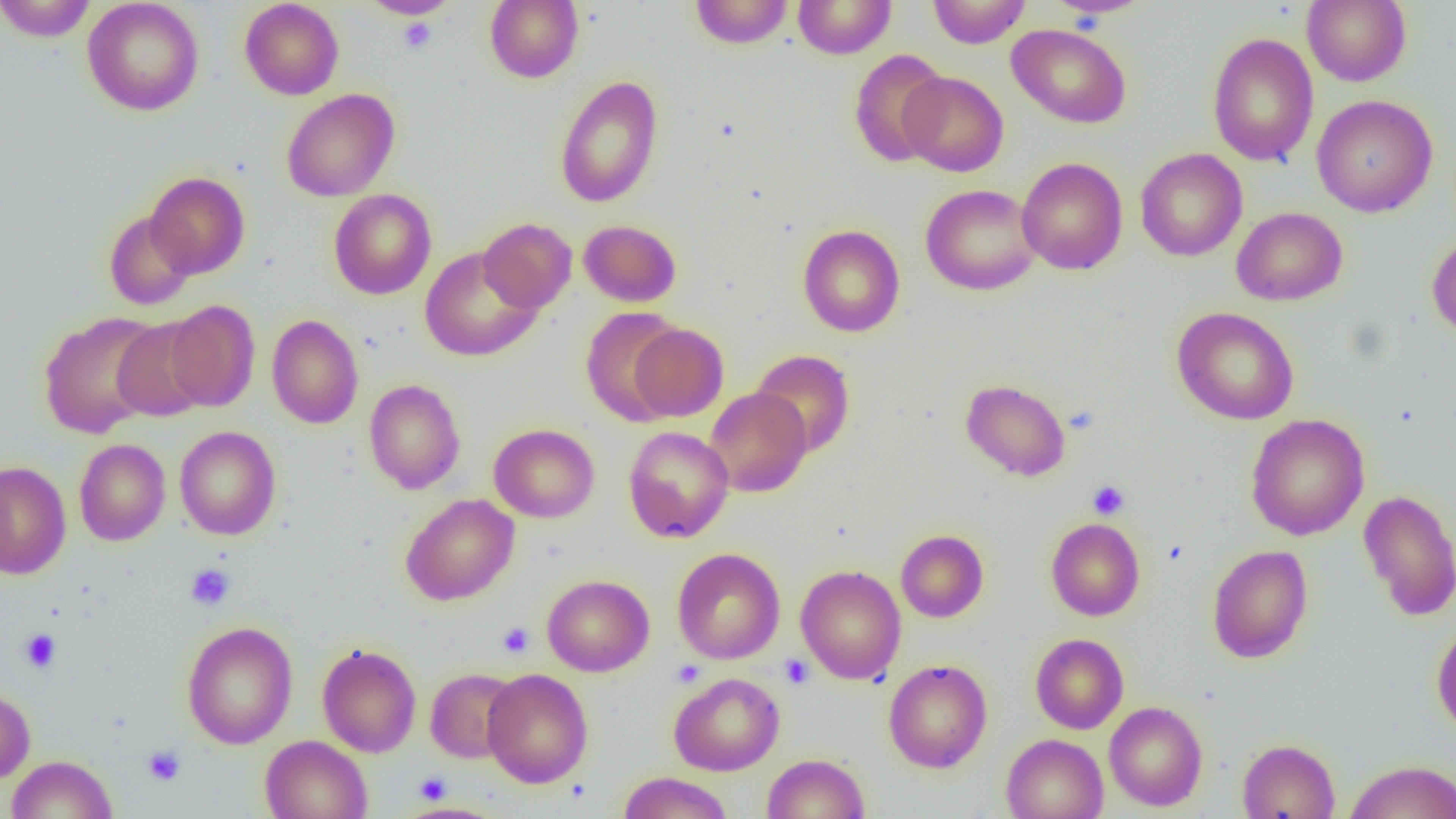

slide-level diagnosis = no evidence of blood parasites
platelet locations = approximate bounding boxes as (x1, y1, x2, y2) in pixels: (396, 16, 438, 54), (1064, 405, 1099, 434), (1087, 480, 1129, 520), (185, 564, 235, 611), (498, 623, 534, 658), (19, 629, 61, 673), (779, 654, 814, 688), (142, 745, 186, 786), (414, 771, 452, 804)
image size = 1456×819 pixels
preparation = thin blood film
uninfected red blood cell locations = approximate bounding boxes as (x1, y1, x2, y2) in pixels: (0, 0, 97, 41), (82, 0, 204, 116), (239, 0, 344, 100), (361, 0, 458, 19), (690, 0, 793, 49), (793, 0, 895, 59), (927, 0, 1031, 48), (1044, 0, 1153, 19), (1301, 0, 1412, 86), (485, 1, 583, 83), (1007, 23, 1132, 128), (1207, 32, 1319, 166), (849, 49, 950, 167), (900, 71, 1008, 176), (554, 74, 664, 209), (281, 88, 400, 202), (1311, 94, 1438, 217), (1135, 148, 1247, 262), (1016, 157, 1127, 275), (145, 172, 250, 278), (920, 183, 1041, 296), (328, 189, 437, 300), (1231, 207, 1347, 306), (103, 210, 196, 310), (478, 218, 577, 313), (579, 220, 682, 307), (797, 225, 905, 337), (1427, 234, 1456, 339), (419, 246, 542, 361), (164, 300, 261, 411), (580, 307, 686, 426), (1172, 307, 1299, 424), (38, 311, 164, 438), (164, 312, 362, 418), (266, 314, 363, 428), (112, 319, 213, 422), (629, 323, 728, 422), (750, 349, 856, 458), (364, 378, 465, 494), (960, 379, 1071, 481), (705, 388, 812, 497), (1245, 414, 1369, 540), (489, 423, 599, 523), (175, 426, 281, 539), (623, 426, 734, 542), (74, 439, 171, 546), (0, 461, 71, 579), (1358, 488, 1456, 621), (400, 493, 520, 606), (1046, 518, 1145, 621), (896, 529, 989, 623), (1207, 544, 1313, 663), (672, 547, 785, 664), (795, 564, 906, 684), (542, 574, 654, 677), (182, 620, 298, 749), (1431, 622, 1456, 737), (1030, 633, 1128, 734), (317, 643, 421, 757), (883, 659, 993, 773), (425, 668, 521, 763), (482, 668, 593, 788), (668, 672, 784, 775), (0, 689, 35, 783), (1104, 701, 1208, 811), (1001, 733, 1108, 819), (260, 735, 372, 819), (1237, 739, 1340, 818), (763, 753, 870, 819), (7, 755, 118, 818), (1344, 760, 1456, 819), (617, 772, 733, 819)
modality = optical microscopy
field of view = one of a larger specimen
magnification = 1000x